Point out each Plasmodium parasite.
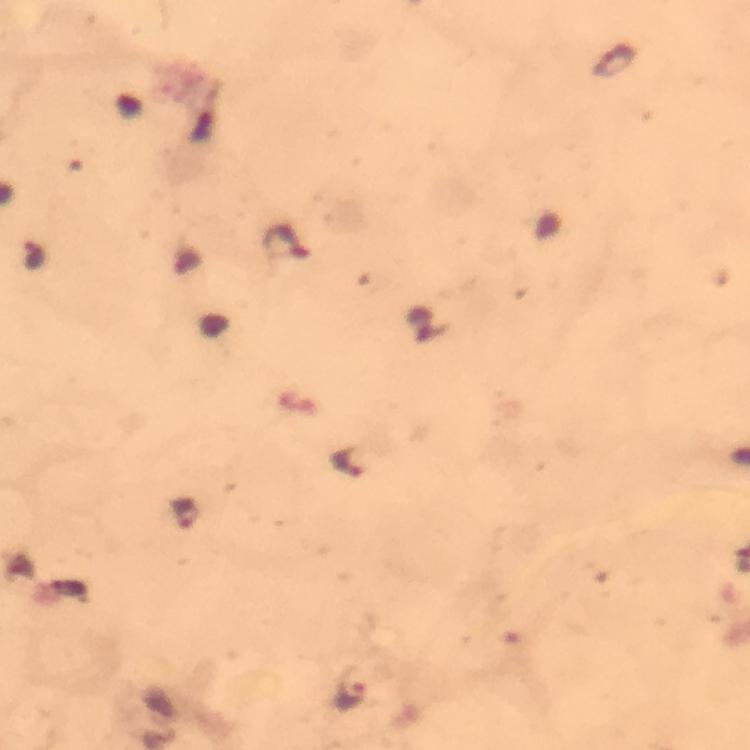

Approximate centers as {x, y} in pixels.
Plasmodium parasites: {616, 61}, {284, 240}, {348, 463}, {184, 513}, {352, 686}.

Summary:
  - Magnification: 100x
  - Cropped from: one field of view
  - Image size: 750×750 pixels
  - Preparation: thick smear
  - Context: from a malaria diagnostic workup
  - Capture: smartphone photograph through a microscope
  - Stain: Giemsa
  - Immersion oil: used